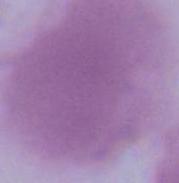
Captured at 1000x magnification. An erythrocyte is shown. Micrograph.